Assess this cell for malaria.
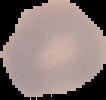
Uninfected.

image size = 106×100 pixels
preparation = thin blood smear
image type = cell region segmented out of the field of view; surrounding area masked to black